Outline each blood parasite and name the species.
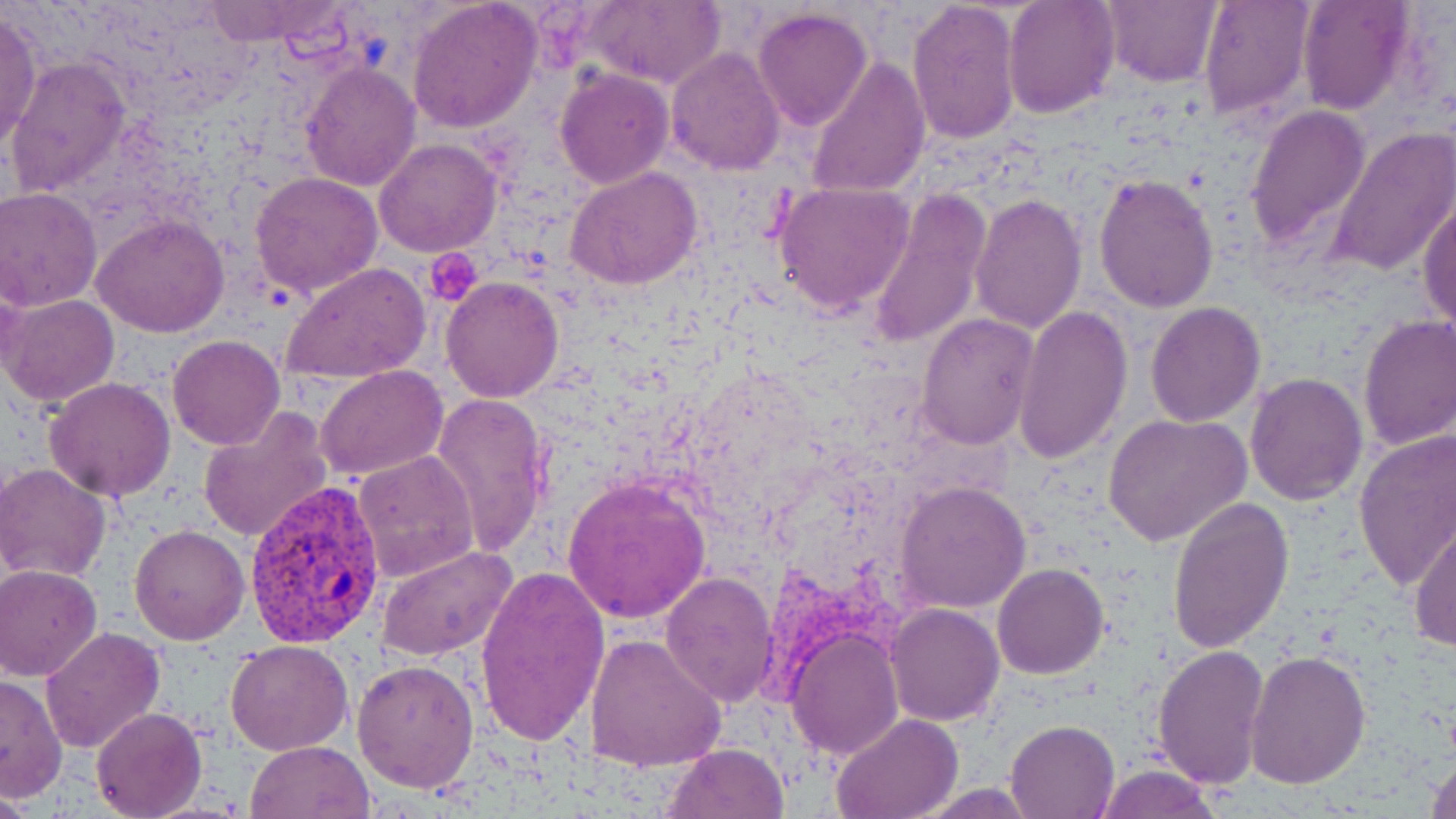
Approximate bounding boxes as (x1, y1, x2, y2) in pixels.
Plasmodium vivax-infected red blood cells: (243, 480, 385, 649).
No Plasmodium falciparum, Plasmodium ovale, Plasmodium malariae, Babesia divergens, or Trypanosoma brucei observed.

Summary:
  - Platelet locations: (423, 248, 483, 308)
  - Uninfected red blood cell locations: (406, 0, 543, 133), (906, 0, 1020, 148), (1002, 0, 1121, 119), (1101, 0, 1220, 88), (1197, 0, 1313, 123), (1296, 0, 1416, 115), (198, 1, 342, 46), (579, 1, 724, 90), (753, 5, 874, 131), (0, 9, 44, 158), (665, 46, 784, 175), (4, 55, 131, 200), (808, 56, 932, 199), (300, 62, 420, 192), (554, 68, 673, 190), (1243, 102, 1372, 251), (1329, 127, 1456, 275), (374, 138, 502, 258), (566, 166, 703, 290), (250, 172, 386, 296), (1093, 172, 1220, 312), (773, 182, 916, 318), (0, 186, 103, 311), (868, 190, 992, 352), (970, 193, 1086, 332), (1416, 195, 1456, 330), (91, 212, 229, 338), (284, 262, 431, 386), (441, 276, 565, 402), (3, 292, 120, 406), (1146, 300, 1266, 427), (1013, 306, 1132, 464), (1357, 312, 1456, 452), (917, 313, 1038, 449), (167, 334, 284, 449), (316, 365, 447, 481), (1244, 371, 1367, 505), (44, 376, 177, 502), (431, 390, 552, 558), (198, 407, 334, 543), (1102, 414, 1252, 547), (1354, 432, 1456, 593), (351, 451, 479, 582), (1, 464, 114, 582), (562, 476, 711, 624), (896, 480, 1033, 613), (1167, 497, 1294, 653), (1409, 522, 1456, 653), (130, 524, 249, 644), (375, 544, 517, 660), (993, 563, 1108, 679), (0, 565, 103, 681), (474, 566, 609, 749), (660, 573, 777, 703), (884, 602, 1005, 726), (40, 627, 165, 754), (786, 631, 904, 759), (584, 633, 728, 772), (224, 640, 352, 756), (1151, 643, 1269, 789), (1244, 648, 1372, 789), (353, 658, 478, 795), (1, 673, 67, 802), (91, 707, 207, 819), (830, 713, 963, 819), (1005, 718, 1121, 818), (247, 741, 375, 819), (663, 743, 789, 819), (1424, 752, 1456, 819), (1090, 765, 1222, 818)
  - Slide-level diagnosis: Plasmodium vivax
  - Stain: May-Grünwald-Giemsa
  - Image size: 1456×819 pixels
  - Field of view: one of a larger specimen
  - Preparation: thin blood smear
  - Magnification: 1000x
  - Modality: optical microscopy